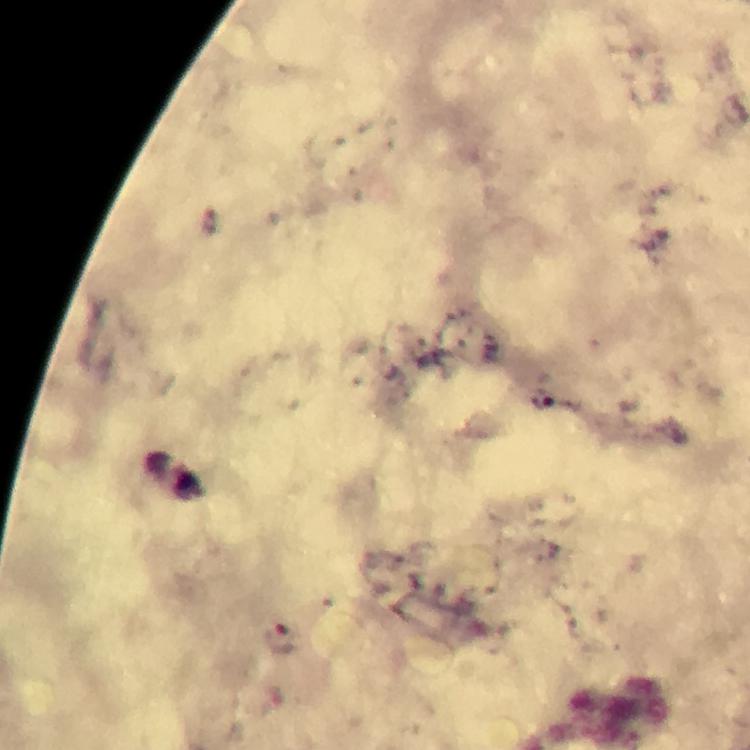
Approximate centers as [x, y] in pixels. Plasmodium parasite locations: [213, 222], [541, 399], [279, 636]. A crop from one field of view. Immersion oil applied. Giemsa stain. Image is 750×750 pixels. From a malaria diagnostic workup. Photographed through the microscope with a smartphone camera. At 100x magnification. Thick smear.